Report the malaria status of this cell.
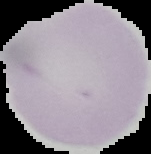
Uninfected.

From a thin blood smear. The area outside the segmented cell region is set to black. Image is 151×154 pixels.